Outline every parasitised red blood cell, every trophozoite, every gametocyte, every leukocyte, and every artifact (platelet-like body, stain precipitate, or debris).
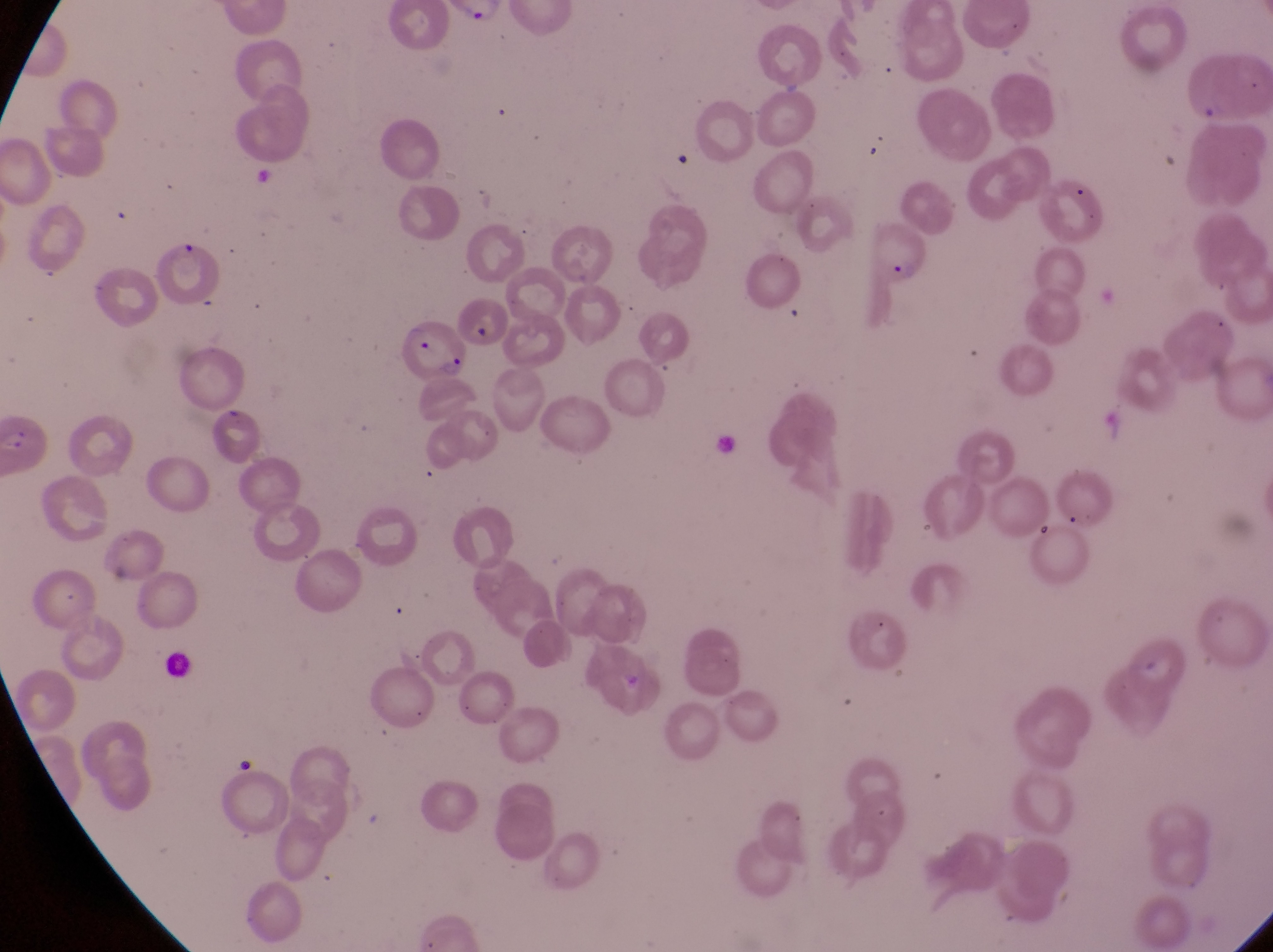
Approximate bounding boxes as [left, top, right, bottom] in pixels.
Parasitised red blood cells: [863, 223, 937, 291], [452, 289, 510, 349], [399, 313, 473, 383].
No leukocytes observed.

Summary:
  - Magnification: 1000x
  - Capture: smartphone photograph through the eyepiece of an Olympus CX-23 microscope
  - Preparation: thin blood smear
  - Field of view: single
  - Image size: 1273×952 pixels
  - Country: Uganda